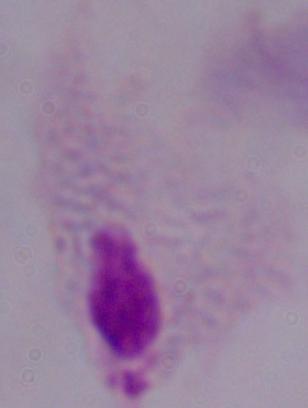

Micrograph. A trichomonad is seen. Captured at 1000x magnification.